Name the cell type shown.
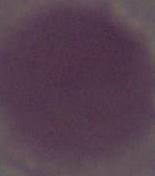

This is an erythrocyte.

Summary:
  - Modality: micrograph
  - Magnification: 1000x